Give the preparation type.
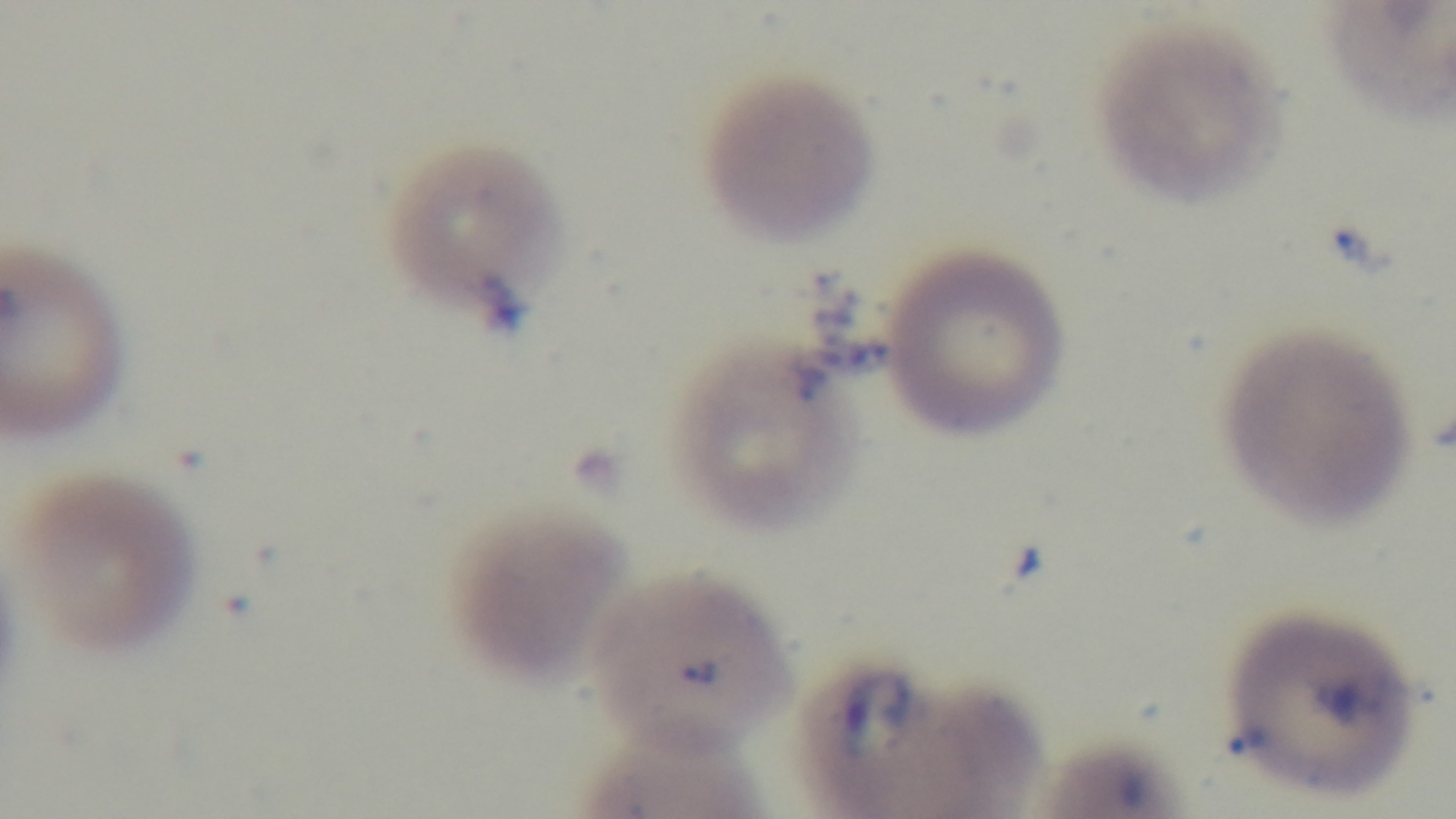
A thin smear.

Summary:
  - Modality: light microscopy
  - Capture: mounted 4K digital camera
  - Malaria status: infected
  - Objective: 100x oil immersion
  - Field of view: single
  - Stain: Giemsa